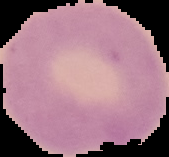

malaria status = uninfected
preparation = thin blood smear
image type = cell region segmented out of the field of view; surrounding area masked to black
image size = 169×157 pixels